Outline each blood parasite and name the species.
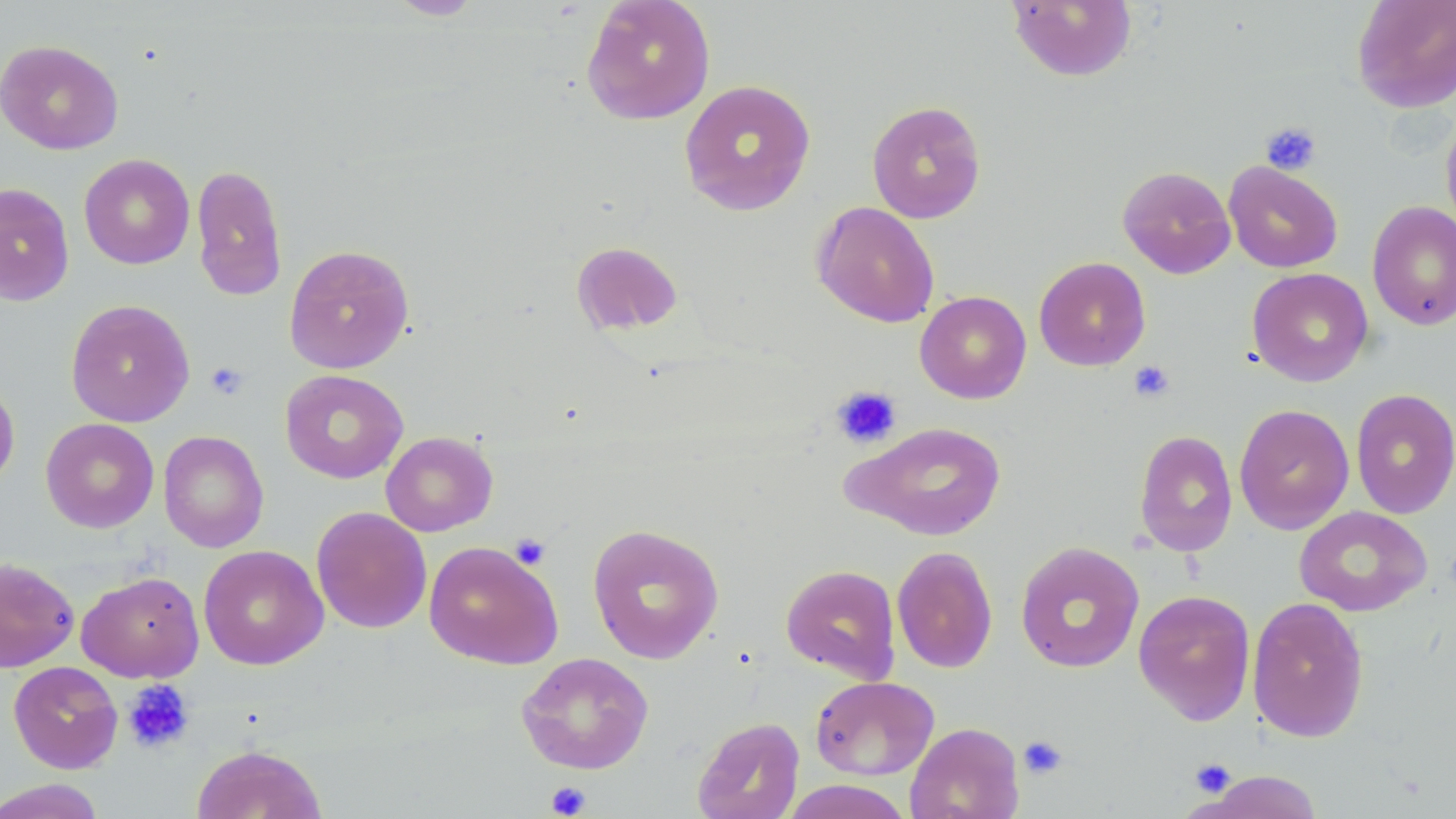
No blood parasites observed.

Approximate bounding boxes as named x1/y1/x2/y2 corners in pixels. Platelet locations: (x1=1261, y1=121, x2=1322, y2=175), (x1=1128, y1=360, x2=1175, y2=403), (x1=205, y1=362, x2=249, y2=400), (x1=831, y1=385, x2=902, y2=449), (x1=510, y1=533, x2=551, y2=569), (x1=122, y1=680, x2=195, y2=754), (x1=1018, y1=735, x2=1068, y2=779), (x1=1190, y1=758, x2=1236, y2=797), (x1=545, y1=781, x2=591, y2=818). Uninfected red blood cell locations: (x1=385, y1=0, x2=486, y2=20), (x1=1005, y1=0, x2=1138, y2=82), (x1=1351, y1=0, x2=1456, y2=113), (x1=580, y1=1, x2=716, y2=125), (x1=0, y1=39, x2=123, y2=155), (x1=678, y1=78, x2=816, y2=217), (x1=866, y1=100, x2=986, y2=223), (x1=1440, y1=111, x2=1456, y2=238), (x1=79, y1=153, x2=195, y2=269), (x1=1223, y1=161, x2=1343, y2=273), (x1=191, y1=164, x2=288, y2=300), (x1=1118, y1=165, x2=1236, y2=279), (x1=0, y1=182, x2=74, y2=307), (x1=812, y1=201, x2=939, y2=327), (x1=1367, y1=201, x2=1456, y2=330), (x1=571, y1=241, x2=683, y2=335), (x1=283, y1=244, x2=415, y2=374), (x1=1033, y1=256, x2=1151, y2=371), (x1=1247, y1=267, x2=1374, y2=387), (x1=915, y1=290, x2=1032, y2=404), (x1=65, y1=299, x2=195, y2=427), (x1=279, y1=369, x2=408, y2=484), (x1=0, y1=376, x2=20, y2=492), (x1=1351, y1=388, x2=1456, y2=519), (x1=1234, y1=404, x2=1355, y2=535), (x1=41, y1=417, x2=159, y2=533), (x1=847, y1=421, x2=1007, y2=540), (x1=158, y1=430, x2=269, y2=553), (x1=1134, y1=430, x2=1238, y2=557), (x1=380, y1=431, x2=498, y2=537), (x1=1294, y1=505, x2=1433, y2=617), (x1=311, y1=506, x2=432, y2=634), (x1=587, y1=523, x2=725, y2=664), (x1=423, y1=540, x2=563, y2=670), (x1=1015, y1=541, x2=1145, y2=673), (x1=198, y1=545, x2=328, y2=670), (x1=892, y1=545, x2=998, y2=674), (x1=0, y1=557, x2=80, y2=672), (x1=780, y1=564, x2=901, y2=683), (x1=76, y1=570, x2=205, y2=682), (x1=1133, y1=589, x2=1256, y2=726), (x1=1247, y1=596, x2=1369, y2=742), (x1=516, y1=651, x2=655, y2=774), (x1=8, y1=660, x2=123, y2=774), (x1=810, y1=675, x2=939, y2=780), (x1=692, y1=716, x2=805, y2=818), (x1=904, y1=722, x2=1024, y2=819), (x1=191, y1=744, x2=327, y2=819), (x1=1201, y1=770, x2=1325, y2=818), (x1=0, y1=778, x2=107, y2=818), (x1=782, y1=780, x2=915, y2=818). Slide-level diagnosis: no evidence of blood parasites. Light microscopy. Image is 1456×819 pixels. Single field of view. 1000x magnification. May-Grünwald-Giemsa stain. Thin blood film.